Assess this cell for malaria.
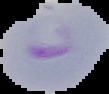
Parasitized.

Image is 109×94 pixels. From a thin blood film. Segmented cell region on a black background.